Name the parasite shown.
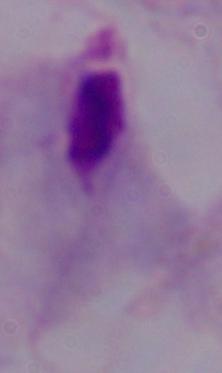

A trichomonad.

modality: micrograph
magnification: 1000x